Describe the morphology of the erythrocytes.
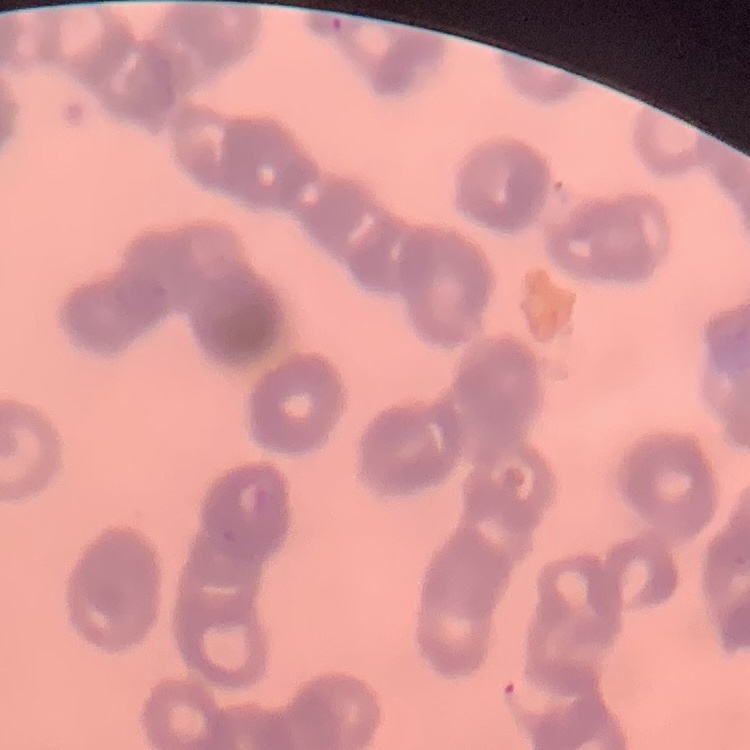

Rouleaux formation.

Field's or Giemsa stain. One tile cut from a larger photomicrograph. Thin peripheral smear.